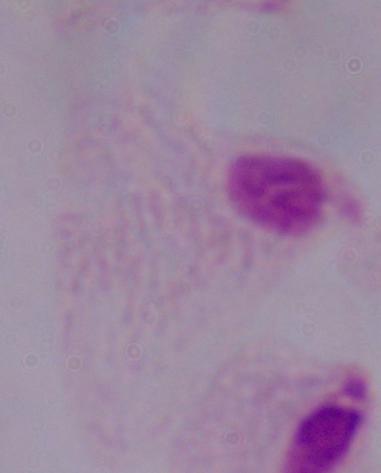
Summary:
  - Magnification: 1000x
  - Modality: micrograph
  - Identification: trichomonad